State which parasite is depicted.
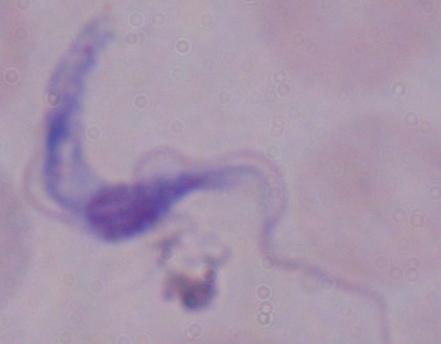

A trypanosome.

Summary:
  - Magnification: 1000x
  - Modality: photomicrograph